Classify this cell by malaria status.
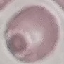

Uninfected.

{
  "stain": "Giemsa",
  "image_type": "automatically extracted cell patch, resized to 64 × 64 pixels",
  "capture": "smartphone camera at the microscope eyepiece",
  "preparation": "thin blood smear"
}